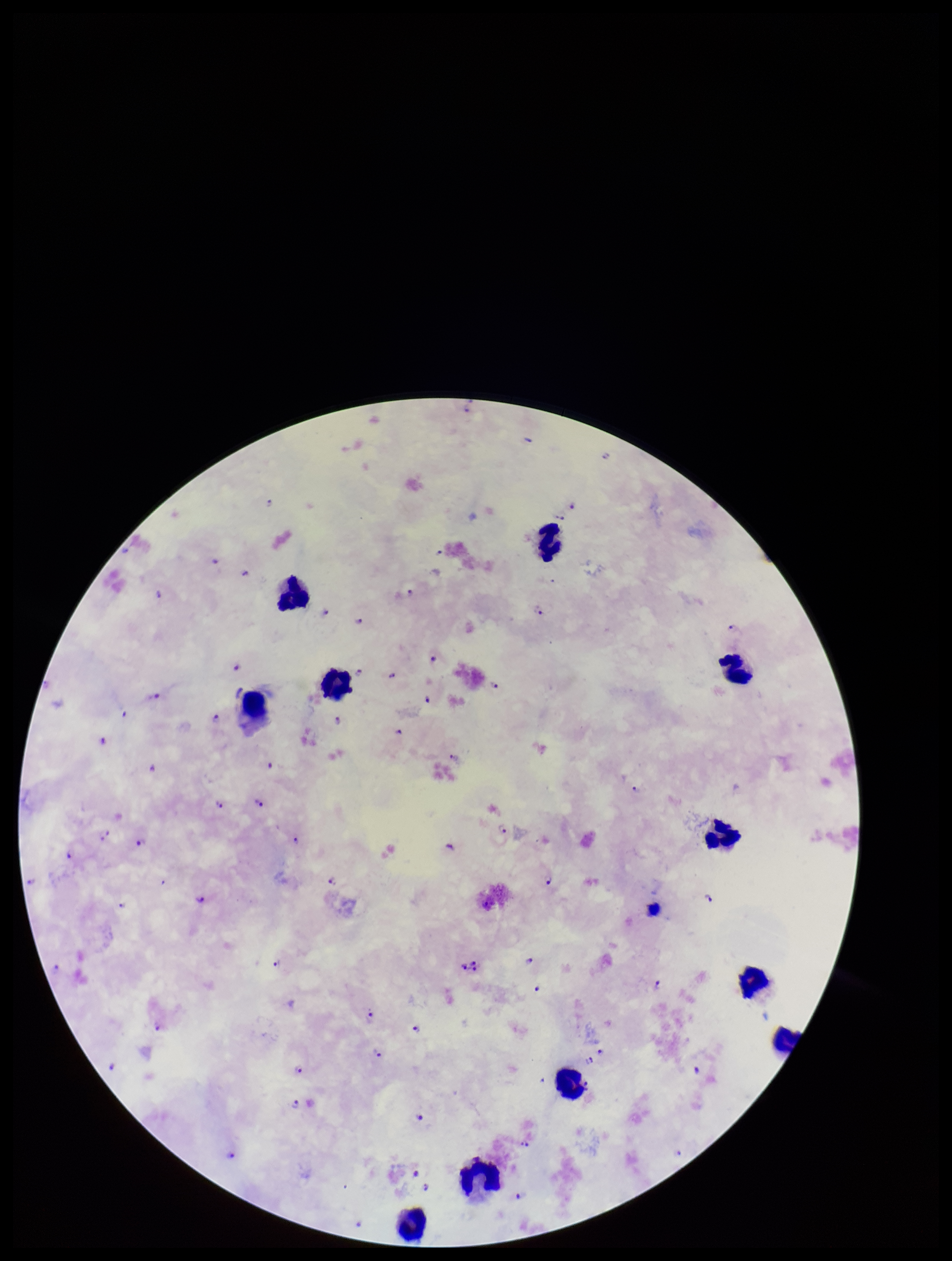

preparation = thick smear
Plasmodium parasites = seen
species reported for this patient = Plasmodium falciparum
image size = 952×1261 pixels
field of view = single
parasite count = 68
capture = smartphone photograph through the microscope eyepiece
stain = Giemsa
leukocyte count = 10
patient malaria status = infected